Locate every Plasmodium vivax-infected red blood cell.
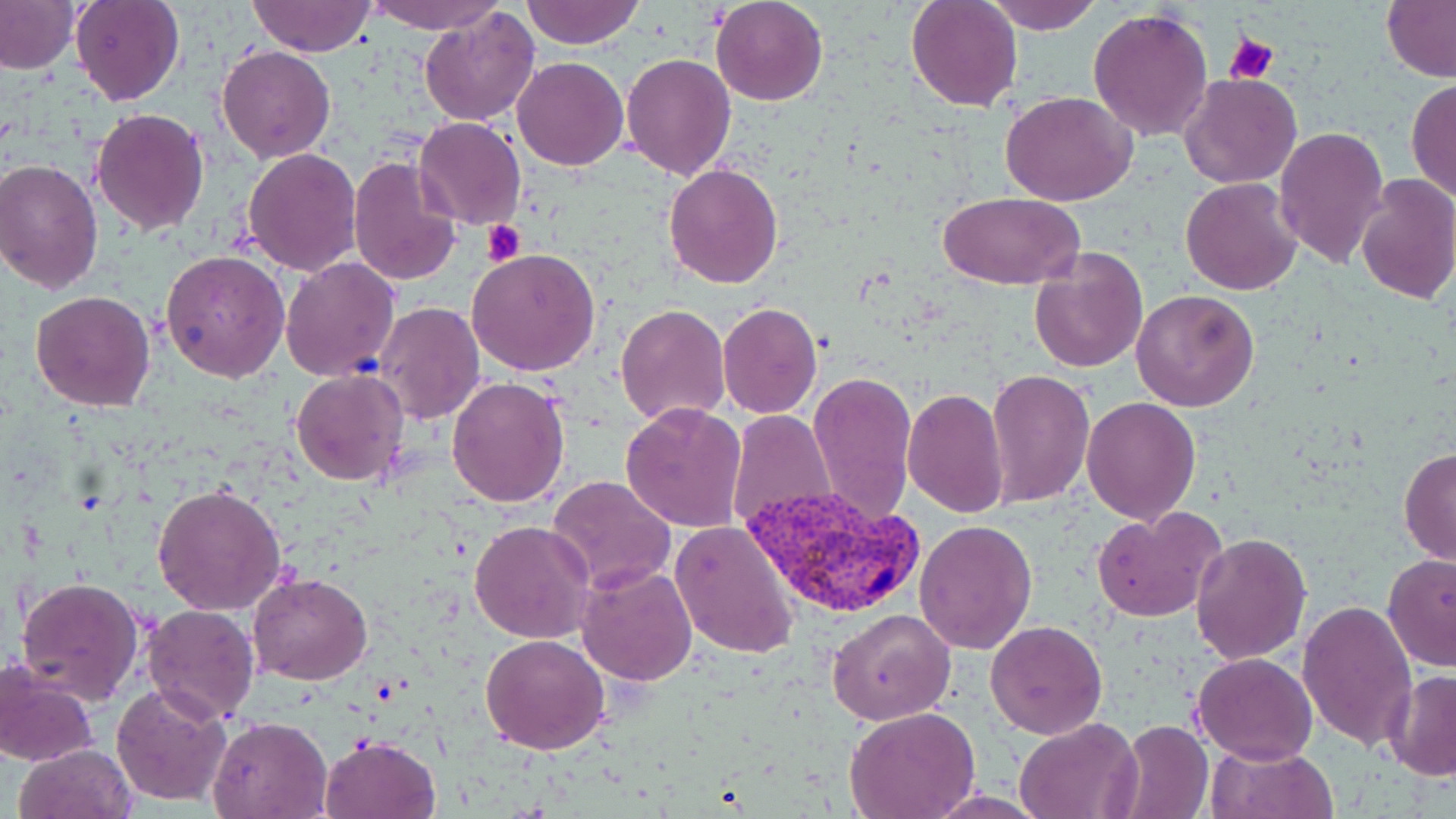

Approximate bounding boxes as (x1, y1, x2, y2) in pixels.
Plasmodium vivax-infected red blood cells: (740, 485, 923, 619).

slide-level diagnosis = Plasmodium vivax
preparation = thin blood smear
magnification = 1000x
field of view = one of a larger specimen
image size = 1456×819 pixels
platelet locations = approximate bounding boxes as (x1, y1, x2, y2) in pixels: (1225, 33, 1278, 85), (482, 220, 526, 265)
uninfected red blood cell locations = approximate bounding boxes as (x1, y1, x2, y2) in pixels: (70, 0, 186, 106), (364, 0, 507, 32), (521, 0, 647, 47), (711, 0, 828, 106), (906, 0, 1023, 112), (986, 0, 1103, 33), (0, 1, 79, 75), (247, 1, 377, 56), (1381, 1, 1456, 83), (420, 7, 540, 127), (1089, 7, 1215, 143), (216, 45, 336, 163), (621, 53, 736, 180), (512, 57, 628, 171), (1180, 74, 1302, 188), (1406, 78, 1456, 203), (1001, 93, 1134, 207), (92, 108, 209, 233), (413, 117, 527, 231), (1275, 127, 1390, 270), (241, 149, 362, 275), (347, 156, 463, 287), (0, 160, 103, 293), (664, 162, 783, 288), (1356, 175, 1456, 305), (1181, 178, 1304, 295), (937, 191, 1086, 289), (1027, 245, 1147, 373), (467, 247, 602, 376), (162, 249, 290, 382), (279, 258, 400, 382), (1131, 288, 1260, 411), (30, 290, 158, 411), (375, 301, 485, 424), (615, 302, 730, 426), (717, 303, 821, 418), (290, 369, 410, 487), (988, 369, 1096, 508), (807, 370, 917, 524), (445, 375, 570, 508), (903, 388, 1008, 516), (1081, 396, 1201, 523), (620, 403, 748, 533), (727, 410, 836, 532), (1398, 447, 1456, 566), (546, 474, 677, 593), (152, 482, 287, 615), (1090, 507, 1225, 622), (914, 517, 1037, 654), (670, 518, 801, 660), (469, 519, 595, 643), (1191, 532, 1311, 665), (1383, 553, 1456, 672), (574, 561, 700, 684), (247, 572, 372, 685), (16, 575, 144, 706), (1296, 600, 1417, 750), (140, 604, 260, 723), (828, 609, 957, 726), (985, 620, 1108, 738), (480, 634, 611, 755), (1194, 652, 1318, 764), (0, 658, 100, 766), (1383, 671, 1456, 780), (111, 683, 232, 808), (846, 706, 980, 818), (208, 716, 331, 818), (1013, 716, 1141, 819), (1115, 718, 1212, 819), (321, 733, 440, 819), (14, 743, 137, 819), (1204, 743, 1338, 819)
stain = May-Grünwald-Giemsa
modality = optical microscopy